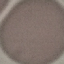
{
  "result": "no malaria parasites seen",
  "preparation": "thin blood smear",
  "stain": "Giemsa",
  "capture": "smartphone camera at the microscope eyepiece",
  "image_type": "cell patch, automatically extracted from a larger field of view and resized to 64 × 64 pixels"
}